Outline each P. falciparum parasite and classify it by life-cycle stage.
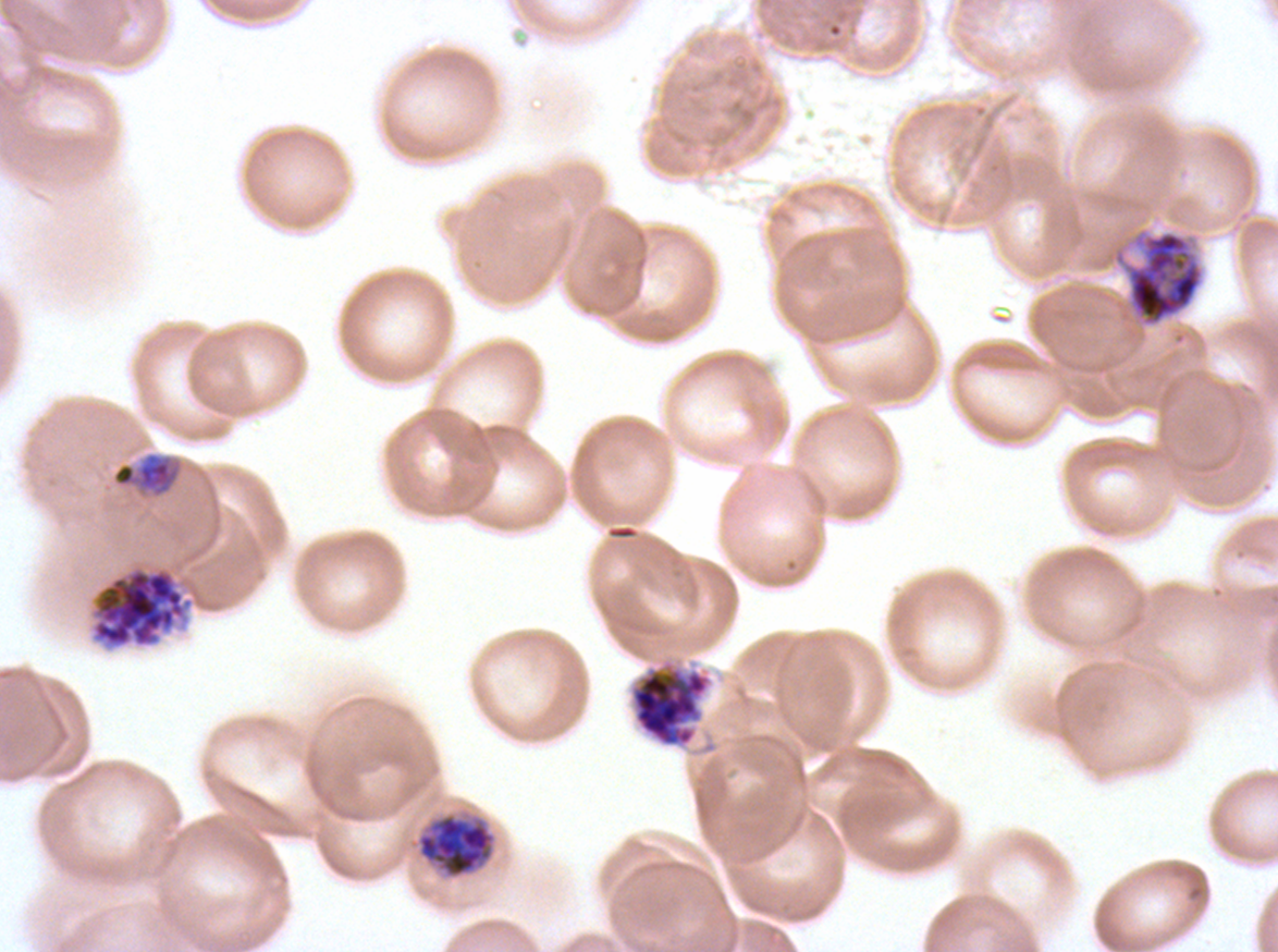

Approximate bounding boxes as (x1, y1, x2, y2) in pixels.
Mid trophozoites: (111, 451, 184, 499).
Early schizonts: (1111, 226, 1206, 328), (629, 660, 712, 748).
Segmenters: (89, 564, 201, 650).
No rings, late-ring/early-trophozoite forms, late trophozoites, late schizonts, or gametocytes observed.

Summary:
  - Image size: 1278×952 pixels
  - Life-cycle stages observed: mid trophozoite, early schizont, segmenter
  - Stain: Giemsa
  - Preparation: thin blood smear
  - Field of view: one sub-image of a larger composite
  - Specimen: P. falciparum from a patient in The Gambia, cultured ex vivo for 24 to 48 hours